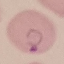
malaria status = parasitized
stain = Giemsa
capture = smartphone through the microscope eyepiece
preparation = thin blood smear
image type = automatically extracted cell patch, resized to 64 × 64 pixels